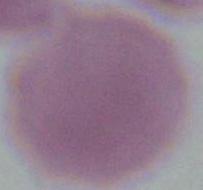
magnification: 1000x
modality: photomicrograph
identification: red blood cell